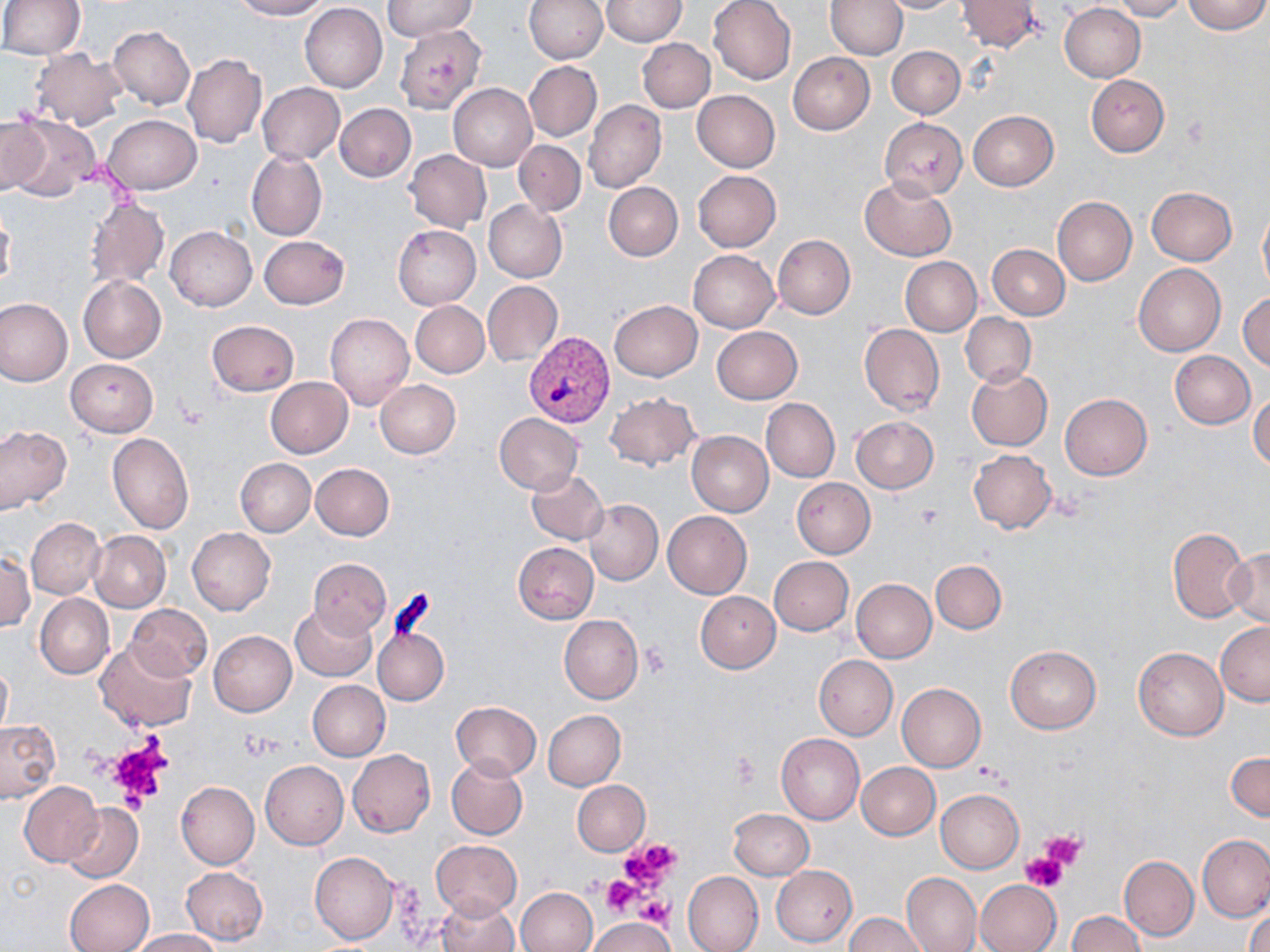
Approximate bounding boxes as named x1/y1/x2/y2 corners in pixels. Uninfected red blood cell locations: (x1=231, y1=0, x2=328, y2=20), (x1=383, y1=0, x2=478, y2=42), (x1=524, y1=0, x2=607, y2=64), (x1=601, y1=0, x2=687, y2=46), (x1=709, y1=0, x2=796, y2=85), (x1=826, y1=0, x2=907, y2=59), (x1=878, y1=0, x2=963, y2=13), (x1=1111, y1=0, x2=1189, y2=21), (x1=1182, y1=0, x2=1269, y2=34), (x1=0, y1=1, x2=84, y2=58), (x1=957, y1=1, x2=1040, y2=51), (x1=300, y1=3, x2=388, y2=92), (x1=1058, y1=3, x2=1146, y2=82), (x1=108, y1=26, x2=195, y2=110), (x1=395, y1=27, x2=484, y2=113), (x1=638, y1=37, x2=715, y2=113), (x1=887, y1=46, x2=965, y2=118), (x1=29, y1=48, x2=129, y2=131), (x1=788, y1=52, x2=874, y2=134), (x1=182, y1=53, x2=266, y2=148), (x1=524, y1=60, x2=601, y2=142), (x1=518, y1=63, x2=590, y2=217), (x1=1086, y1=75, x2=1169, y2=156), (x1=257, y1=83, x2=345, y2=164), (x1=448, y1=84, x2=537, y2=170), (x1=691, y1=90, x2=779, y2=173), (x1=584, y1=100, x2=666, y2=194), (x1=335, y1=103, x2=416, y2=182), (x1=967, y1=111, x2=1059, y2=191), (x1=103, y1=114, x2=201, y2=194), (x1=0, y1=115, x2=47, y2=194), (x1=6, y1=116, x2=98, y2=198), (x1=879, y1=118, x2=967, y2=199), (x1=514, y1=139, x2=586, y2=215), (x1=246, y1=149, x2=327, y2=241), (x1=406, y1=149, x2=491, y2=232), (x1=693, y1=170, x2=781, y2=251), (x1=861, y1=177, x2=956, y2=262), (x1=604, y1=182, x2=682, y2=261), (x1=1147, y1=186, x2=1236, y2=264), (x1=1052, y1=196, x2=1137, y2=286), (x1=85, y1=199, x2=168, y2=289), (x1=485, y1=200, x2=567, y2=282), (x1=1258, y1=204, x2=1270, y2=298), (x1=1, y1=213, x2=15, y2=293), (x1=392, y1=225, x2=481, y2=310), (x1=165, y1=226, x2=256, y2=311), (x1=773, y1=235, x2=855, y2=318), (x1=258, y1=236, x2=349, y2=310), (x1=987, y1=245, x2=1069, y2=320), (x1=688, y1=249, x2=779, y2=333), (x1=901, y1=257, x2=981, y2=335), (x1=1133, y1=263, x2=1225, y2=356), (x1=78, y1=276, x2=167, y2=363), (x1=482, y1=280, x2=563, y2=367), (x1=1238, y1=290, x2=1270, y2=371), (x1=0, y1=298, x2=73, y2=388), (x1=609, y1=300, x2=702, y2=381), (x1=410, y1=301, x2=489, y2=377), (x1=960, y1=312, x2=1035, y2=386), (x1=325, y1=313, x2=415, y2=411), (x1=206, y1=320, x2=298, y2=397), (x1=858, y1=324, x2=944, y2=415), (x1=712, y1=326, x2=802, y2=404), (x1=1169, y1=350, x2=1256, y2=428), (x1=65, y1=358, x2=158, y2=437), (x1=966, y1=368, x2=1052, y2=451), (x1=265, y1=377, x2=352, y2=457), (x1=374, y1=379, x2=461, y2=459), (x1=1250, y1=390, x2=1270, y2=470), (x1=604, y1=392, x2=698, y2=470), (x1=1060, y1=394, x2=1151, y2=480), (x1=760, y1=398, x2=840, y2=482), (x1=494, y1=412, x2=584, y2=495), (x1=850, y1=416, x2=938, y2=494), (x1=0, y1=426, x2=71, y2=513), (x1=687, y1=430, x2=774, y2=516), (x1=107, y1=432, x2=193, y2=533), (x1=968, y1=449, x2=1057, y2=534), (x1=234, y1=458, x2=315, y2=536), (x1=311, y1=464, x2=395, y2=540), (x1=527, y1=469, x2=608, y2=545), (x1=791, y1=478, x2=875, y2=558), (x1=585, y1=500, x2=663, y2=585), (x1=662, y1=511, x2=751, y2=599), (x1=27, y1=519, x2=104, y2=598), (x1=1168, y1=526, x2=1251, y2=623), (x1=187, y1=527, x2=275, y2=615), (x1=88, y1=530, x2=171, y2=612), (x1=513, y1=542, x2=599, y2=624), (x1=1225, y1=548, x2=1270, y2=628), (x1=2, y1=552, x2=35, y2=633), (x1=770, y1=556, x2=854, y2=636), (x1=307, y1=558, x2=392, y2=636), (x1=931, y1=560, x2=1006, y2=633), (x1=852, y1=578, x2=936, y2=663), (x1=695, y1=591, x2=780, y2=673), (x1=35, y1=594, x2=114, y2=679), (x1=126, y1=603, x2=212, y2=682), (x1=290, y1=604, x2=377, y2=682), (x1=559, y1=615, x2=643, y2=703), (x1=1215, y1=621, x2=1270, y2=705), (x1=374, y1=626, x2=449, y2=706), (x1=209, y1=630, x2=296, y2=716), (x1=96, y1=639, x2=196, y2=732), (x1=1005, y1=645, x2=1101, y2=734), (x1=1133, y1=647, x2=1228, y2=740), (x1=814, y1=654, x2=897, y2=739), (x1=0, y1=662, x2=11, y2=739), (x1=307, y1=680, x2=390, y2=761), (x1=897, y1=683, x2=986, y2=771), (x1=452, y1=702, x2=541, y2=779), (x1=543, y1=710, x2=625, y2=790), (x1=0, y1=720, x2=59, y2=803), (x1=776, y1=733, x2=864, y2=824), (x1=347, y1=749, x2=436, y2=837), (x1=1227, y1=751, x2=1269, y2=822), (x1=447, y1=757, x2=527, y2=840), (x1=261, y1=760, x2=349, y2=849), (x1=856, y1=761, x2=940, y2=840), (x1=572, y1=779, x2=650, y2=856), (x1=176, y1=781, x2=259, y2=869), (x1=19, y1=783, x2=102, y2=866), (x1=936, y1=789, x2=1023, y2=872), (x1=62, y1=803, x2=143, y2=882), (x1=728, y1=808, x2=814, y2=880), (x1=1197, y1=835, x2=1269, y2=923), (x1=431, y1=840, x2=522, y2=918), (x1=310, y1=851, x2=398, y2=944), (x1=1120, y1=856, x2=1198, y2=940), (x1=771, y1=865, x2=857, y2=947), (x1=181, y1=866, x2=267, y2=945), (x1=683, y1=871, x2=763, y2=952), (x1=901, y1=872, x2=982, y2=952), (x1=64, y1=878, x2=154, y2=952), (x1=975, y1=879, x2=1062, y2=952), (x1=517, y1=888, x2=598, y2=952), (x1=436, y1=895, x2=519, y2=952), (x1=1246, y1=909, x2=1270, y2=952), (x1=1068, y1=911, x2=1145, y2=952), (x1=844, y1=912, x2=929, y2=951), (x1=585, y1=915, x2=673, y2=952), (x1=130, y1=930, x2=219, y2=952). Platelet locations: (x1=915, y1=506, x2=944, y2=529), (x1=639, y1=644, x2=670, y2=676), (x1=240, y1=733, x2=285, y2=761), (x1=106, y1=738, x2=173, y2=807), (x1=729, y1=753, x2=760, y2=788), (x1=972, y1=764, x2=1007, y2=787), (x1=1041, y1=831, x2=1087, y2=870), (x1=619, y1=837, x2=682, y2=890), (x1=1022, y1=853, x2=1068, y2=892), (x1=600, y1=876, x2=643, y2=917), (x1=637, y1=895, x2=671, y2=932). Plasmodium vivax-infected red blood cell locations: (x1=523, y1=331, x2=615, y2=427). Slide-level diagnosis: Plasmodium vivax. Optical microscopy. Thin blood film. Image is 1270×952 pixels. May-Grünwald-Giemsa-stained preparation. One field of a larger specimen. Captured at 1000x magnification.